Identify the parasite.
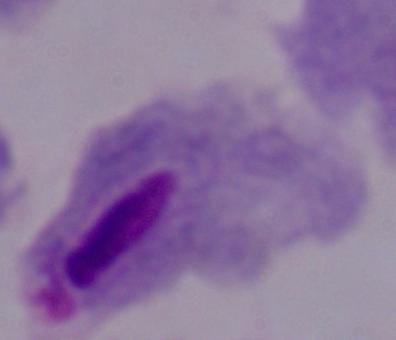

A trichomonad.

Summary:
  - Modality: photomicrograph
  - Magnification: 1000x